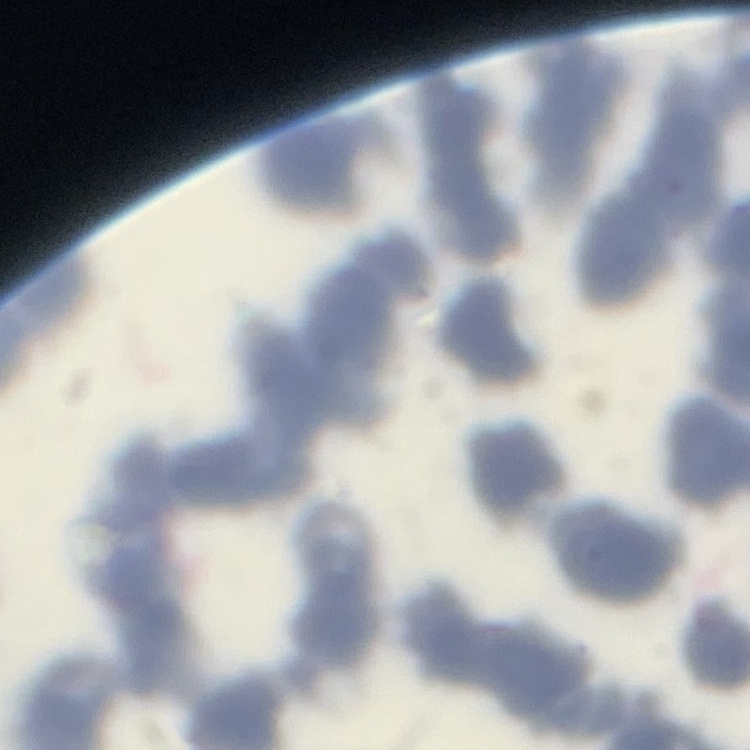

erythrocyte morphology = rouleaux formation
stain = Field's or Giemsa
preparation = thin blood smear
image type = square crop of a larger photomicrograph